Assess the morphology of the red blood cells.
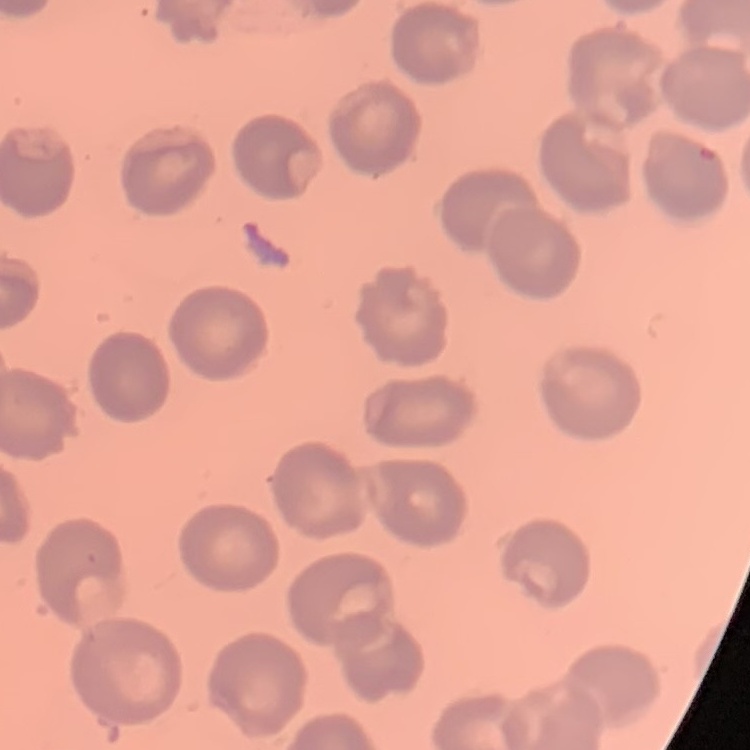

No rouleaux formation.

Field's or Giemsa stain. One tile cut from a larger photomicrograph. Thin peripheral smear.